Outline each blood parasite and name the species.
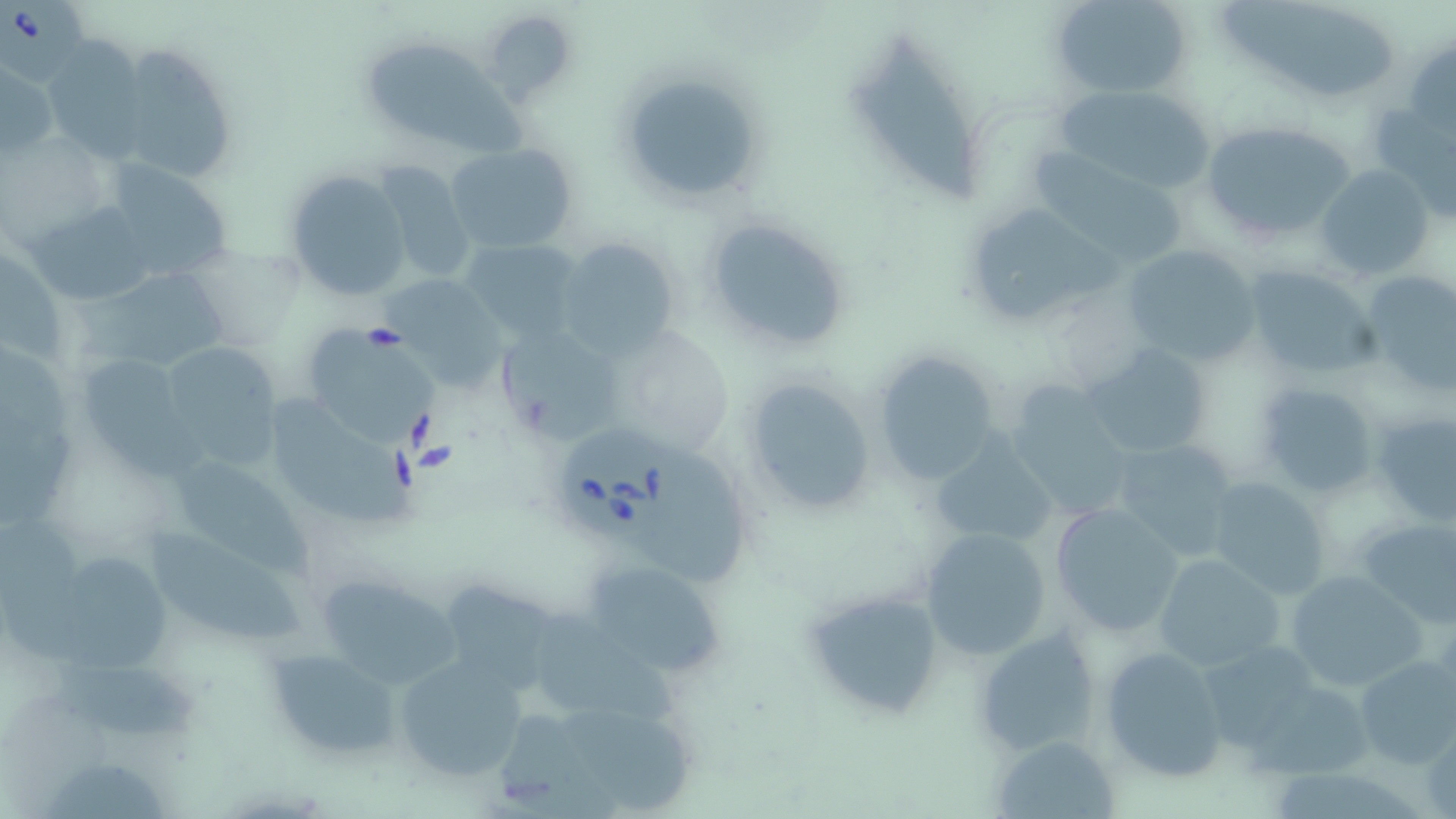

Approximate bounding boxes as (x1,y1)-(x2,y2) corner pairs in pixels.
Babesia divergens-infected red blood cells: (0,0)-(89,85), (559,426)-(688,539).
No Plasmodium falciparum, Plasmodium ovale, Plasmodium malariae, Plasmodium vivax, or Trypanosoma brucei observed.

{
  "slide_level_diagnosis": "Babesia divergens",
  "modality": "light microscopy",
  "magnification": "1000x",
  "uninfected_red_blood_cell_locations": "approximate bounding boxes as (x1,y1)-(x2,y2) corner pairs in pixels: (1049,0)-(1193,97), (1220,0)-(1398,105), (479,8)-(578,105), (846,32)-(985,204), (41,36)-(151,162), (1406,38)-(1456,140), (363,43)-(525,150), (131,48)-(236,182), (2,62)-(56,160), (615,67)-(765,206), (1048,81)-(1221,197), (1196,119)-(1361,247), (445,140)-(579,253), (1023,147)-(1191,266), (96,157)-(241,286), (369,159)-(479,288), (1316,164)-(1435,280), (284,168)-(413,305), (23,202)-(155,302), (962,202)-(1124,332), (699,211)-(855,356), (555,236)-(682,357), (461,237)-(585,342), (1123,242)-(1261,369), (1243,265)-(1383,380), (1355,270)-(1456,398), (75,279)-(239,363), (495,322)-(622,444), (603,323)-(737,456), (300,328)-(442,451), (166,344)-(283,471), (1083,344)-(1214,458), (871,352)-(1000,484), (79,354)-(218,481), (739,376)-(879,520), (1255,381)-(1379,497), (1002,382)-(1133,519), (273,394)-(416,530), (1368,412)-(1455,526), (931,434)-(1057,553), (1107,436)-(1242,562), (177,464)-(316,579), (1204,476)-(1332,599), (1048,502)-(1186,637), (1351,516)-(1456,625), (918,527)-(1052,660), (149,531)-(312,646), (60,551)-(169,670), (1151,553)-(1288,674), (581,559)-(729,680), (1283,568)-(1430,695), (318,573)-(462,694), (446,582)-(571,688), (800,584)-(947,722), (534,610)-(684,723), (974,625)-(1103,756), (1198,641)-(1327,753), (262,644)-(403,761), (1099,644)-(1230,782), (393,655)-(526,781), (1354,656)-(1456,770), (48,665)-(206,744), (560,706)-(698,812), (501,715)-(626,819), (990,737)-(1121,817), (47,756)-(172,819)",
  "image_size": "1456×819 pixels",
  "preparation": "thin blood smear",
  "stain": "May-Grünwald-Giemsa",
  "field_of_view": "one of a larger specimen"
}